Outline each blood parasite and name the species.
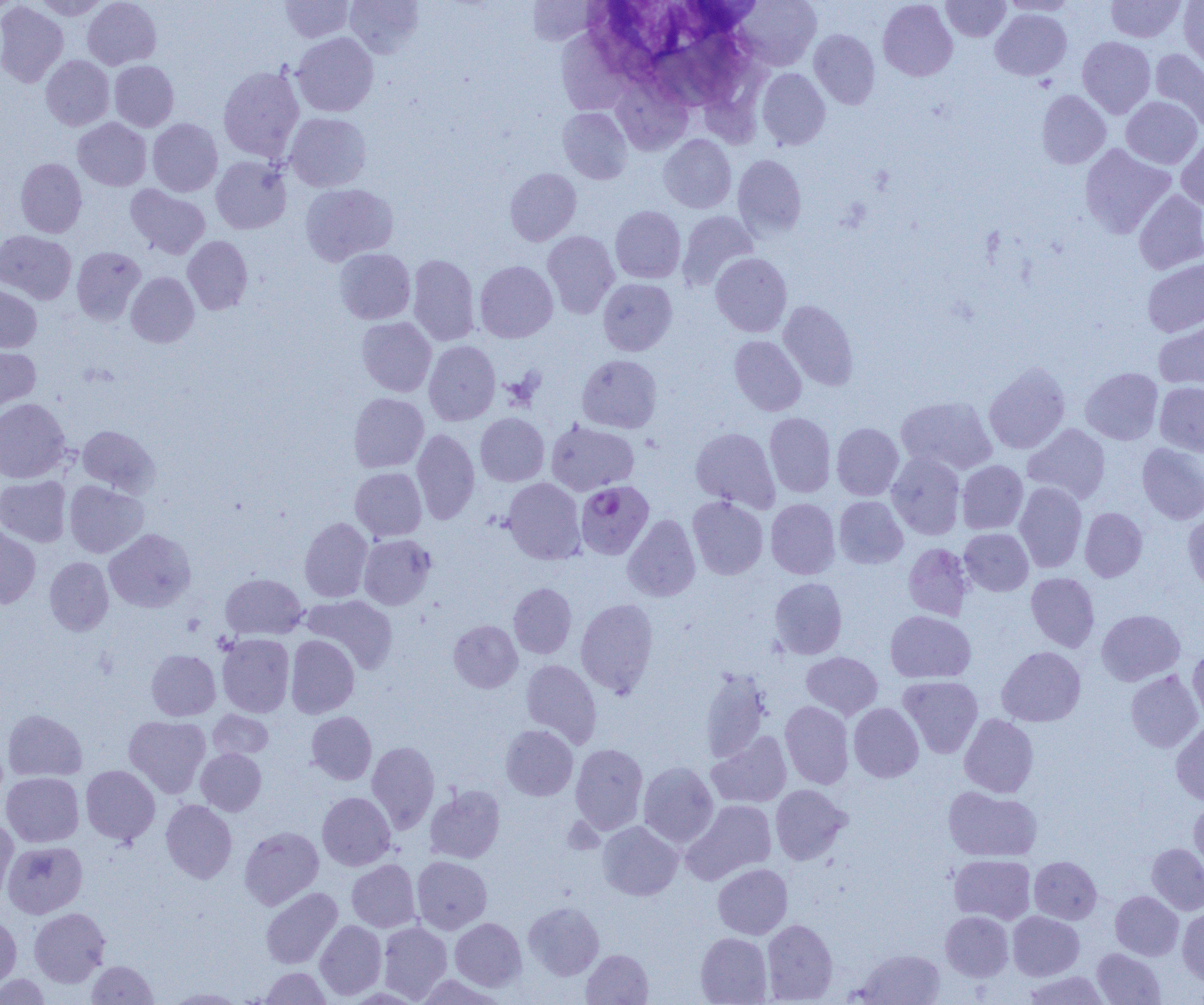

Approximate bounding boxes as named x1/y1/x2/y2 corners in pixels.
Plasmodium falciparum-infected red blood cells: (x1=576, y1=480, x2=654, y2=560).
No Plasmodium ovale, Plasmodium malariae, Plasmodium vivax, Babesia divergens, or Trypanosoma brucei observed.

slide_level_diagnosis: Plasmodium falciparum
image_size: 1204×1005 pixels
magnification: 1000x
modality: optical microscopy
uninfected_red_blood_cell_locations_subset: 'approximate bounding boxes as named x1/y1/x2/y2 corners in pixels: (x1=31, y1=0, x2=111, y2=19), (x1=83, y1=0, x2=161, y2=69), (x1=280, y1=0, x2=353, y2=42), (x1=345, y1=0, x2=424, y2=58), (x1=524, y1=0, x2=600, y2=46), (x1=736, y1=0, x2=821, y2=70), (x1=878, y1=0, x2=957, y2=81), (x1=942, y1=0, x2=1010, y2=41), (x1=1000, y1=0, x2=1080, y2=16), (x1=1106, y1=0, x2=1186, y2=43), (x1=1179, y1=0, x2=1204, y2=71), (x1=0, y1=2, x2=68, y2=87), (x1=991, y1=9, x2=1072, y2=81), (x1=560, y1=28, x2=635, y2=112), (x1=809, y1=29, x2=880, y2=109), (x1=292, y1=32, x2=379, y2=116), (x1=1077, y1=36, x2=1156, y2=118), (x1=1150, y1=49, x2=1204, y2=133), (x1=41, y1=55, x2=114, y2=130), (x1=109, y1=60, x2=179, y2=132), (x1=217, y1=65, x2=304, y2=162), (x1=757, y1=68, x2=830, y2=150), (x1=611, y1=78, x2=692, y2=155), (x1=1036, y1=90, x2=1111, y2=169), (x1=1121, y1=96, x2=1202, y2=169), (x1=558, y1=107, x2=632, y2=184), (x1=285, y1=112, x2=371, y2=191), (x1=73, y1=118, x2=152, y2=191), (x1=147, y1=118, x2=223, y2=196), (x1=658, y1=134, x2=736, y2=213), (x1=1176, y1=136, x2=1204, y2=211), (x1=1079, y1=144, x2=1175, y2=238), (x1=732, y1=154, x2=807, y2=239), (x1=211, y1=156, x2=291, y2=234), (x1=15, y1=157, x2=87, y2=237), (x1=505, y1=168, x2=581, y2=246), (x1=300, y1=183, x2=398, y2=266), (x1=126, y1=185, x2=210, y2=259), (x1=1134, y1=189, x2=1204, y2=274), (x1=610, y1=206, x2=686, y2=283), (x1=677, y1=210, x2=758, y2=291), (x1=0, y1=230, x2=76, y2=304), (x1=542, y1=230, x2=619, y2=318), (x1=183, y1=236, x2=253, y2=314), (x1=72, y1=246, x2=146, y2=324), (x1=334, y1=248, x2=415, y2=324), (x1=711, y1=253, x2=792, y2=337), (x1=408, y1=254, x2=480, y2=345), (x1=1142, y1=258, x2=1204, y2=337), (x1=475, y1=260, x2=558, y2=343), (x1=126, y1=272, x2=199, y2=347), (x1=598, y1=278, x2=677, y2=355), (x1=0, y1=284, x2=42, y2=352), (x1=778, y1=300, x2=858, y2=391), (x1=356, y1=317, x2=436, y2=396), (x1=1153, y1=320, x2=1204, y2=389), (x1=729, y1=335, x2=806, y2=416), (x1=424, y1=340, x2=500, y2=425), (x1=0, y1=345, x2=40, y2=415), (x1=577, y1=354, x2=662, y2=433), (x1=983, y1=362, x2=1071, y2=454), (x1=1081, y1=367, x2=1163, y2=445), (x1=1154, y1=381, x2=1204, y2=456), (x1=349, y1=393, x2=428, y2=472), (x1=896, y1=396, x2=998, y2=475), (x1=0, y1=398, x2=70, y2=482), (x1=764, y1=412, x2=836, y2=497), (x1=475, y1=413, x2=549, y2=486), (x1=545, y1=420, x2=639, y2=496), (x1=832, y1=423, x2=904, y2=500), (x1=1023, y1=423, x2=1111, y2=504), (x1=78, y1=425, x2=160, y2=496), (x1=690, y1=427, x2=779, y2=511), (x1=412, y1=428, x2=480, y2=524), (x1=1137, y1=442, x2=1204, y2=524), (x1=886, y1=451, x2=966, y2=540), (x1=957, y1=460, x2=1028, y2=534), (x1=350, y1=467, x2=426, y2=541), (x1=0, y1=475, x2=71, y2=547), (x1=503, y1=477, x2=585, y2=564), (x1=64, y1=481, x2=149, y2=558), (x1=1014, y1=482, x2=1087, y2=573), (x1=687, y1=495, x2=768, y2=580), (x1=834, y1=496, x2=908, y2=568), (x1=766, y1=498, x2=840, y2=579), (x1=1080, y1=507, x2=1147, y2=582), (x1=1183, y1=511, x2=1204, y2=595), (x1=622, y1=514, x2=701, y2=602), (x1=300, y1=517, x2=372, y2=602), (x1=0, y1=523, x2=41, y2=609), (x1=105, y1=528, x2=196, y2=612), (x1=960, y1=528, x2=1033, y2=596), (x1=359, y1=534, x2=435, y2=610), (x1=903, y1=543, x2=974, y2=620), (x1=44, y1=557, x2=113, y2=635), (x1=1026, y1=572, x2=1100, y2=652), (x1=220, y1=573, x2=307, y2=640), (x1=769, y1=577, x2=847, y2=660), (x1=508, y1=583, x2=576, y2=659), (x1=303, y1=595, x2=398, y2=673), (x1=575, y1=598, x2=659, y2=697), (x1=1096, y1=609, x2=1185, y2=685), (x1=885, y1=610, x2=976, y2=683), (x1=449, y1=620, x2=522, y2=692), (x1=217, y1=634, x2=294, y2=717), (x1=286, y1=635, x2=359, y2=719), (x1=996, y1=646, x2=1085, y2=727), (x1=1187, y1=647, x2=1204, y2=724), (x1=146, y1=649, x2=220, y2=720), (x1=801, y1=651, x2=883, y2=720), (x1=521, y1=659, x2=602, y2=748), (x1=699, y1=668, x2=771, y2=763), (x1=1126, y1=670, x2=1203, y2=752), (x1=898, y1=675, x2=983, y2=758), (x1=780, y1=700, x2=854, y2=789), (x1=849, y1=703, x2=924, y2=782), (x1=3, y1=709, x2=87, y2=782), (x1=208, y1=710, x2=273, y2=759), (x1=306, y1=711, x2=377, y2=784), (x1=959, y1=714, x2=1038, y2=797), (x1=124, y1=715, x2=211, y2=798), (x1=1171, y1=720, x2=1204, y2=806), (x1=500, y1=724, x2=578, y2=800), (x1=707, y1=731, x2=792, y2=808), (x1=366, y1=741, x2=439, y2=833), (x1=570, y1=743, x2=648, y2=834), (x1=196, y1=748, x2=266, y2=815), (x1=638, y1=762, x2=718, y2=847), (x1=81, y1=765, x2=160, y2=845), (x1=1, y1=772, x2=84, y2=847), (x1=425, y1=784, x2=505, y2=864), (x1=770, y1=784, x2=851, y2=865), (x1=943, y1=786, x2=1042, y2=862), (x1=317, y1=792, x2=395, y2=870), (x1=161, y1=799, x2=237, y2=884), (x1=682, y1=799, x2=776, y2=884), (x1=1189, y1=799, x2=1204, y2=875), (x1=0, y1=818, x2=19, y2=901), (x1=597, y1=821, x2=683, y2=900), (x1=239, y1=826, x2=323, y2=909), (x1=3, y1=841, x2=87, y2=917), (x1=1146, y1=843, x2=1204, y2=915), (x1=949, y1=854, x2=1036, y2=924), (x1=412, y1=856, x2=492, y2=934), (x1=1029, y1=856, x2=1101, y2=924), (x1=347, y1=859, x2=421, y2=932), (x1=713, y1=863, x2=792, y2=939), (x1=261, y1=887, x2=342, y2=969), (x1=1110, y1=891, x2=1183, y2=960), (x1=524, y1=901, x2=604, y2=979), (x1=29, y1=907, x2=110, y2=987), (x1=1177, y1=907, x2=1204, y2=986), (x1=941, y1=911, x2=1013, y2=981), (x1=1008, y1=911, x2=1084, y2=980), (x1=0, y1=914, x2=21, y2=989), (x1=450, y1=918, x2=527, y2=991), (x1=762, y1=919, x2=838, y2=1004), (x1=315, y1=920, x2=387, y2=1000), (x1=377, y1=921, x2=452, y2=1002), (x1=695, y1=933, x2=772, y2=1004), (x1=1092, y1=948, x2=1166, y2=1004), (x1=582, y1=949, x2=653, y2=1005), (x1=854, y1=949, x2=945, y2=1005), (x1=87, y1=960, x2=157, y2=1004), (x1=260, y1=967, x2=331, y2=1004), (x1=1021, y1=971, x2=1111, y2=1004), (x1=1, y1=974, x2=51, y2=1004), (x1=415, y1=974, x2=505, y2=1005), (x1=165, y1=987, x2=247, y2=1004)'
field_of_view: single
preparation: thin blood film